Evaluate for malaria.
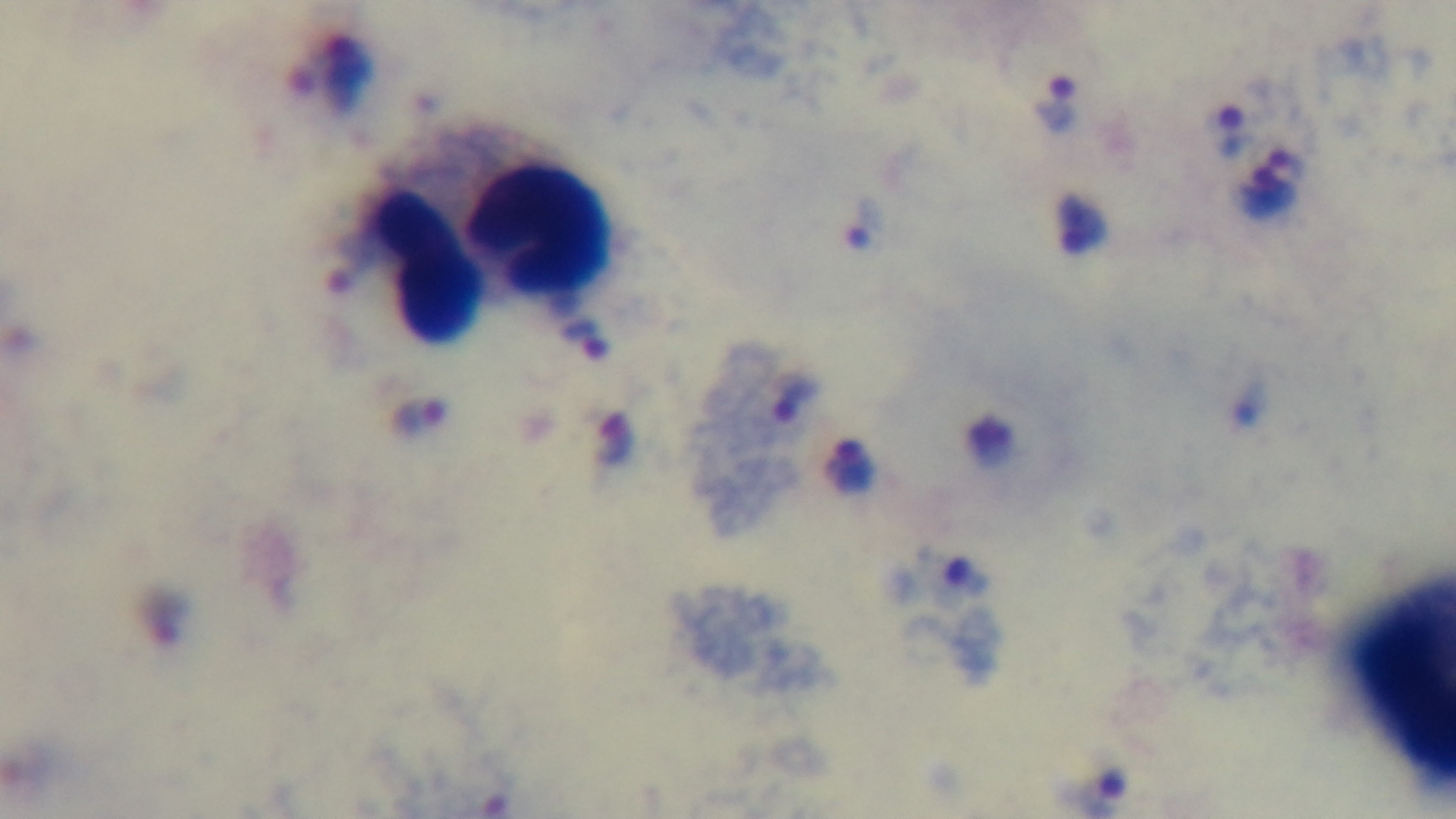

Infected.

Preparation: thick smear. Giemsa-stained. Light microscopy. Mounted 4K digital camera. 100x oil-immersion objective. Single field of view.